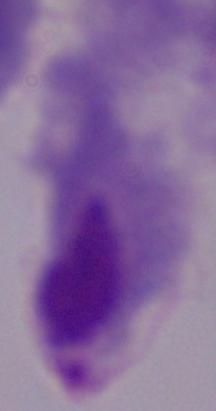
Summary:
  - Magnification: 1000x
  - Identification: trichomonad
  - Modality: photomicrograph